Describe the morphology of the erythrocytes.
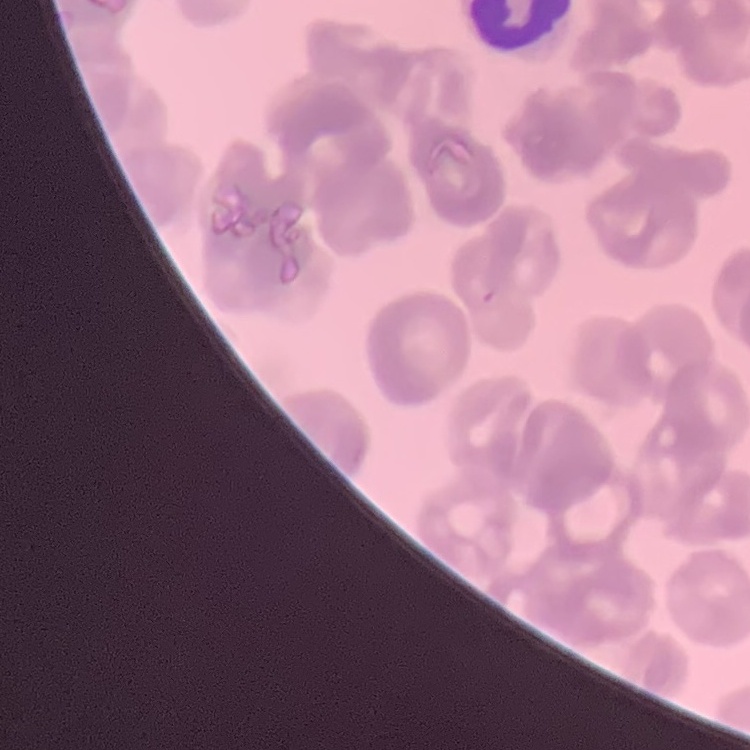

They show rouleaux formation.

Field's or Giemsa stain. Thin peripheral smear. One tile cut from a larger photomicrograph.